Classify this cell by malaria status.
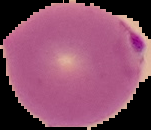
Parasitized.

Segmented cell region on a black background. Image is 151×130 pixels. From a thin blood smear.